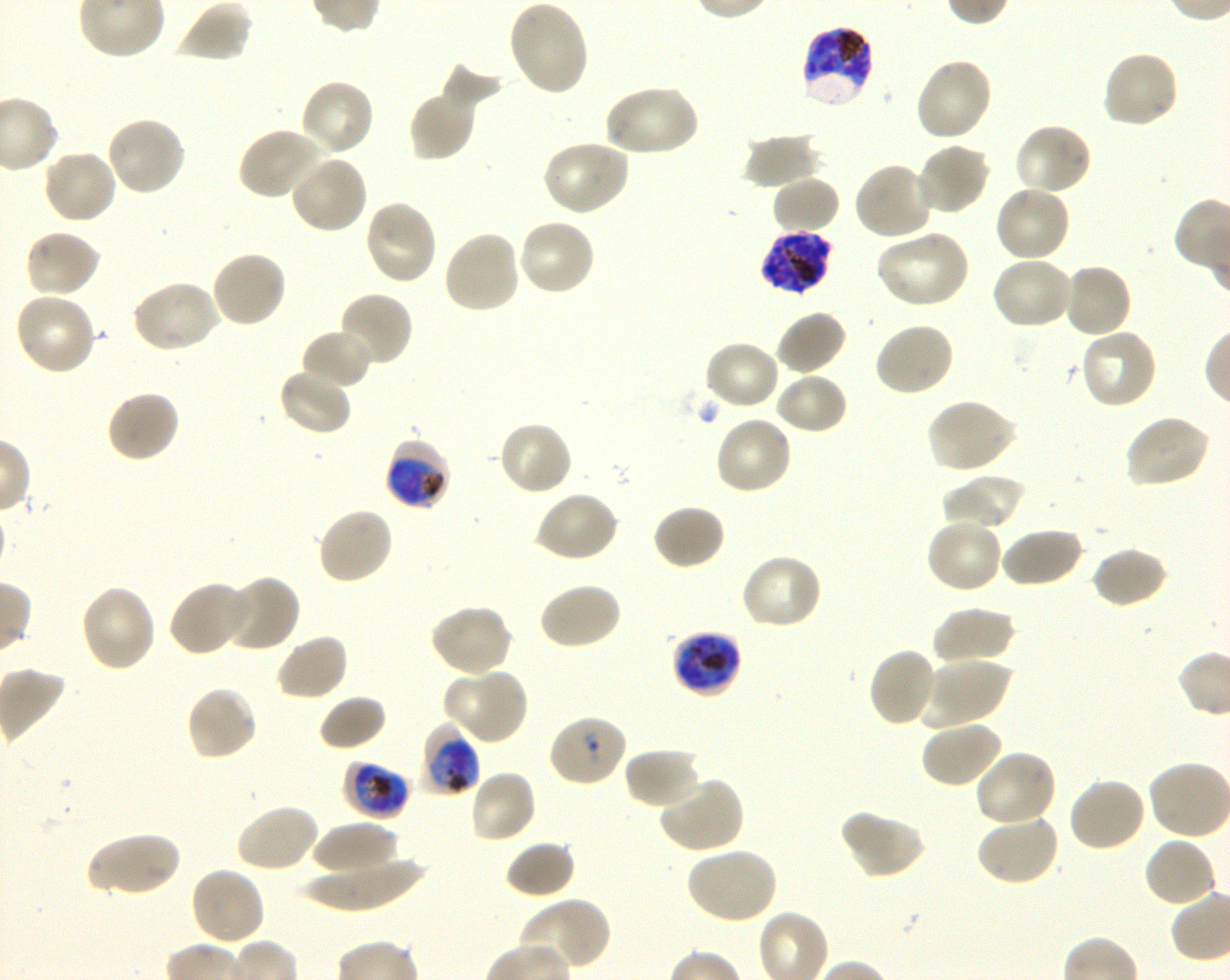
Approximate bounding boxes as [x1, y1, x2, y2] in pixels. Not every red blood cell is marked. A life-cycle stage — or a range of stages, where the recorded stages span more than one — follows each staged infected red blood cell. Locations of infected red blood cells: [800, 25, 876, 110] late trophozoite to late schizont; [759, 231, 832, 296] schizont; [384, 438, 452, 511] trophozoite; [671, 632, 741, 699] late trophozoite to late schizont; [421, 723, 481, 797] trophozoite; [342, 759, 411, 819] late trophozoite to early schizont. Locations of uninfected red blood cells: [507, 0, 590, 97], [178, 2, 252, 63], [1101, 49, 1181, 130], [914, 57, 994, 143], [440, 61, 505, 111], [299, 79, 376, 158], [603, 83, 700, 158], [408, 88, 477, 161], [105, 116, 186, 197], [1013, 122, 1094, 197], [237, 126, 326, 201], [743, 131, 822, 190], [540, 139, 631, 217], [914, 142, 991, 217], [41, 148, 118, 225], [289, 153, 369, 235], [853, 161, 935, 241], [771, 175, 842, 235], [994, 184, 1072, 262], [363, 199, 438, 286], [517, 218, 596, 297], [442, 229, 522, 316], [23, 230, 102, 298], [875, 230, 971, 310], [210, 249, 288, 329], [990, 255, 1075, 331], [1061, 262, 1133, 338], [130, 279, 220, 354], [337, 290, 414, 369], [13, 291, 96, 376], [775, 309, 848, 376], [873, 321, 956, 397], [1079, 327, 1159, 410], [300, 329, 373, 391], [703, 339, 781, 412], [277, 368, 353, 436], [775, 371, 848, 435], [105, 388, 181, 464], [925, 397, 1018, 474], [1124, 414, 1212, 490], [714, 416, 793, 496], [497, 419, 573, 496], [942, 473, 1025, 532], [534, 490, 620, 563], [652, 503, 727, 570], [316, 506, 395, 586], [925, 517, 1004, 594], [999, 527, 1083, 588], [1091, 546, 1169, 608], [739, 553, 823, 630], [222, 573, 301, 653], [167, 581, 252, 656], [538, 582, 622, 651], [79, 584, 157, 672], [429, 604, 513, 678], [932, 608, 1016, 668], [274, 633, 349, 702], [868, 648, 939, 727], [920, 658, 1011, 728], [451, 667, 529, 746], [185, 684, 258, 762], [318, 694, 388, 752], [920, 718, 1004, 788], [623, 747, 702, 809], [974, 749, 1057, 828], [468, 769, 538, 845], [656, 776, 745, 854], [1067, 777, 1147, 853], [235, 803, 320, 874], [840, 808, 927, 882], [976, 814, 1060, 886], [312, 820, 398, 878], [85, 830, 181, 898], [1143, 836, 1217, 908], [504, 840, 576, 899], [684, 846, 779, 925], [300, 856, 428, 912], [189, 866, 266, 946], [518, 898, 610, 974]. Locations of red blood cells of indeterminate infection status: [548, 713, 628, 787]. Life-cycle stages observed: trophozoite, schizont. Giemsa-stained preparation. 100x oil-immersion objective, numerical aperture 1.30. Image is 1230×980 pixels. Thin blood smear. One field from this slide. Plasmodium falciparum strain 3D7 in shaking in-vitro culture. Donor blood group O+.